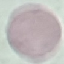
Summary:
  - Malaria status: uninfected
  - Capture: smartphone through the microscope eyepiece
  - Stain: Giemsa
  - Preparation: thin smear
  - Image type: cell patch, automatically extracted from a larger field of view and resized to 64 × 64 pixels